Assess the morphology of the erythrocytes.
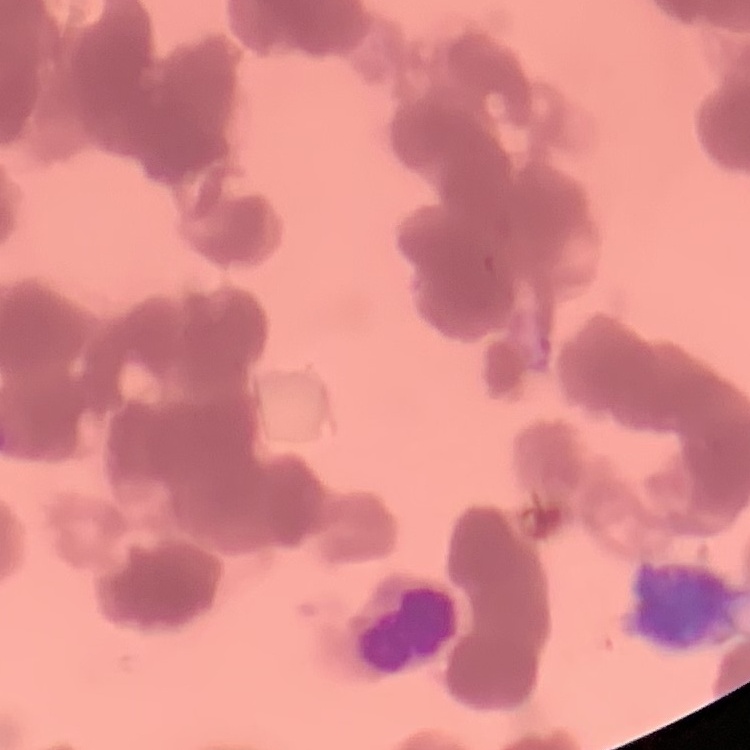

Rouleaux formation.

Thin peripheral smear. One tile cut from a larger photomicrograph. Stained with either Field's or Giemsa.